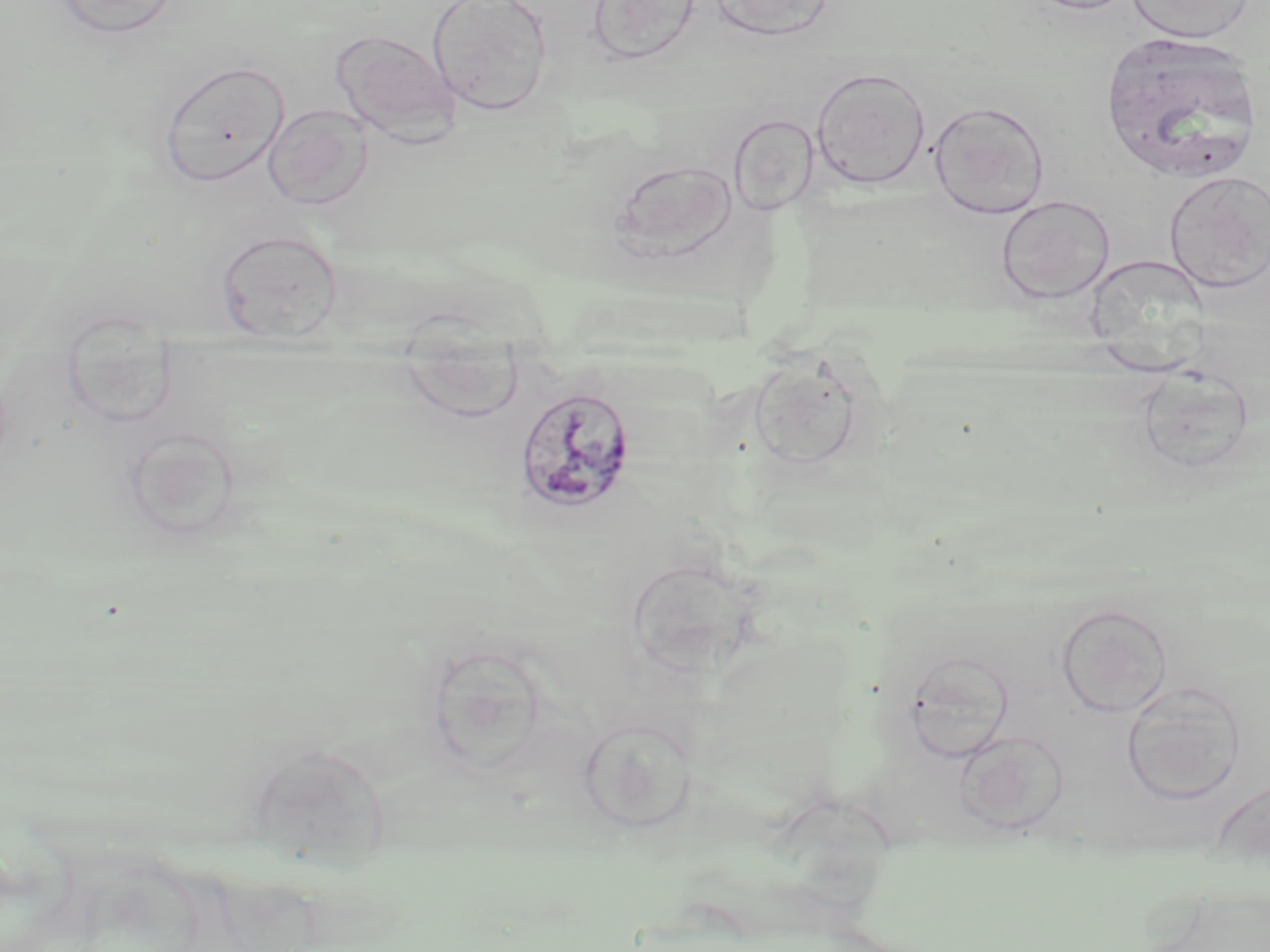
Approximate bounding boxes as (x1,y1)-(x2,y2) corner pairs in pixels. Uninfected red blood cell locations: (427,0)-(553,117), (586,0)-(702,67), (1022,0)-(1138,15), (1126,0)-(1256,44), (51,1)-(182,39), (707,1)-(837,40), (331,30)-(461,144), (1098,31)-(1263,182), (157,59)-(290,188), (810,66)-(931,190), (928,100)-(1050,219), (263,103)-(374,211), (728,113)-(820,216), (608,158)-(739,260), (1164,171)-(1269,292), (996,195)-(1116,304), (215,228)-(343,344), (61,313)-(179,430), (397,335)-(528,423), (743,351)-(873,474), (123,428)-(242,544), (624,555)-(763,676), (1054,602)-(1174,718), (1121,681)-(1246,805), (576,714)-(701,832), (955,730)-(1069,833), (244,741)-(391,865), (1211,779)-(1270,848). Plasmodium malariae-infected red blood cell locations: (514,385)-(638,516). Slide-level diagnosis: Plasmodium malariae. Optical microscopy. Thin blood film. May-Grünwald-Giemsa-stained preparation. One field of a larger specimen. 1000x magnification. Image is 1270×952 pixels.